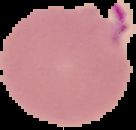
Summary:
  - Image type: segmented cell region on a black background
  - Preparation: thin blood smear
  - Malaria status: parasitized
  - Image size: 136×130 pixels